Name the parasite shown.
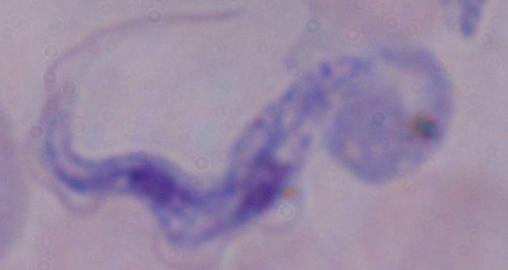
This is a trypanosome.

Summary:
  - Modality: photomicrograph
  - Magnification: 1000x